Comment on the morphology of the erythrocytes.
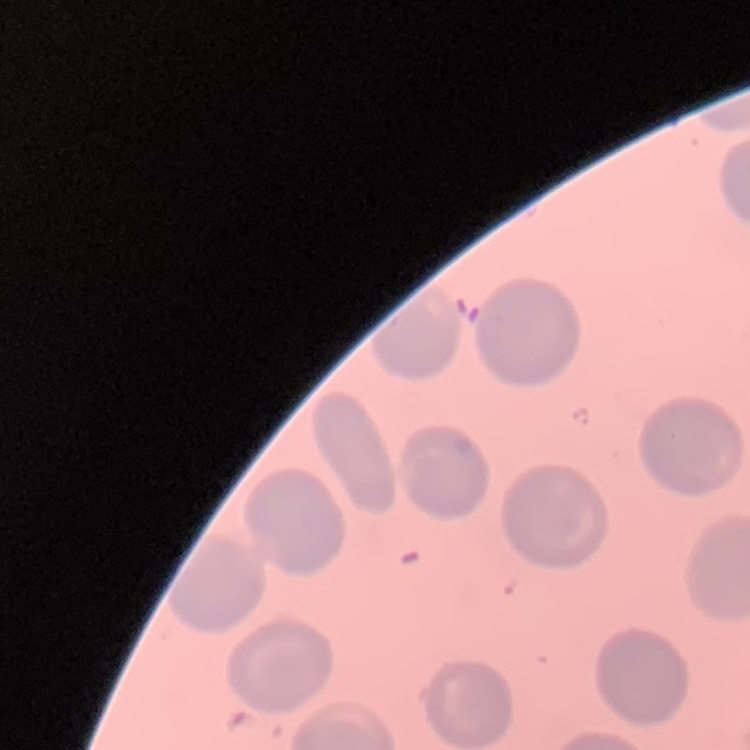
They show no rouleaux formation.

image type = square crop of a larger photomicrograph
stain = Field's or Giemsa
preparation = thin blood smear